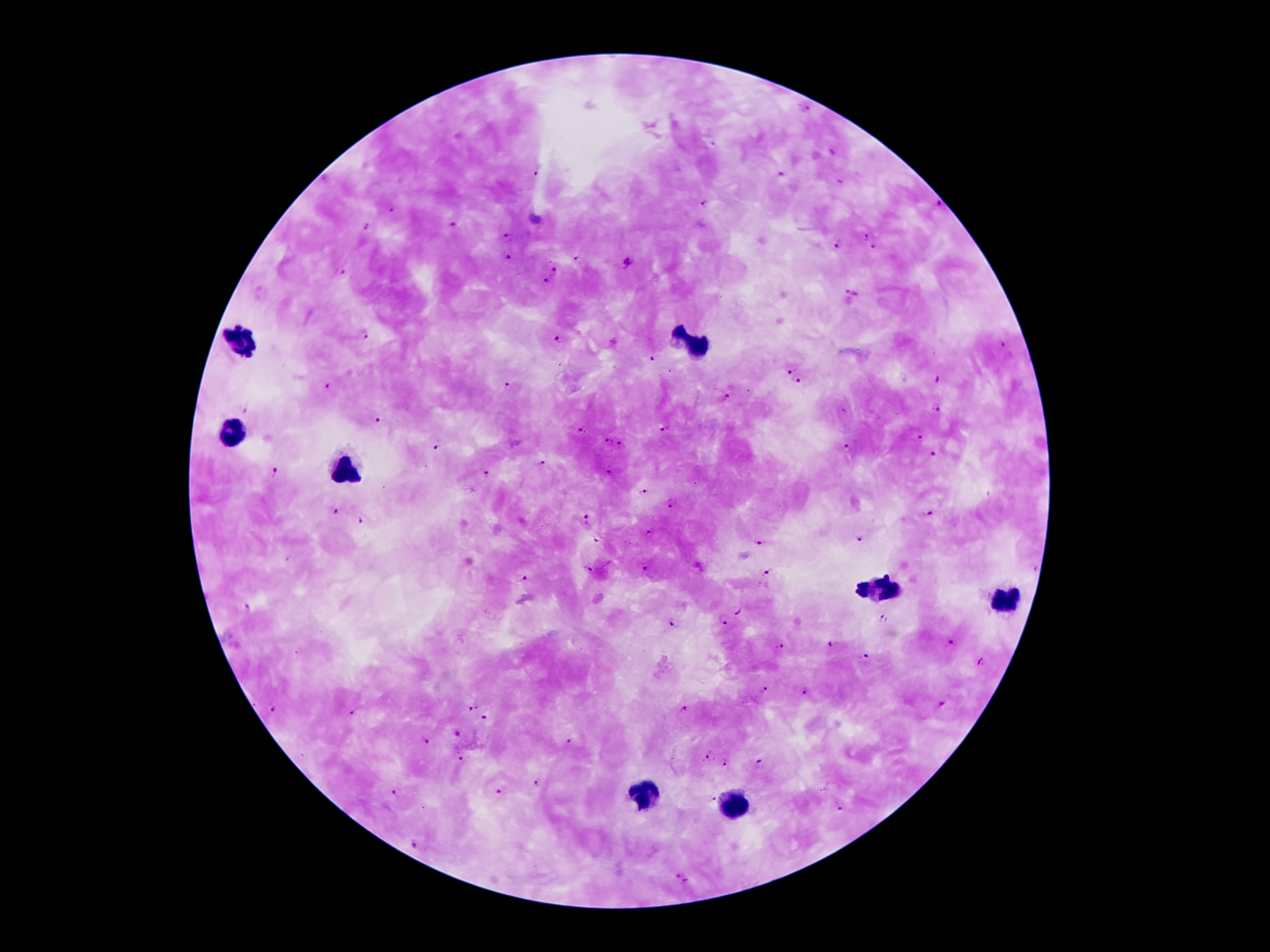
coordinate format = approximate centers as [x, y] in pixels
malaria parasite locations = [804, 109], [539, 170], [780, 173], [705, 204], [939, 205], [392, 210], [455, 226], [367, 228], [509, 236], [866, 239], [837, 246], [874, 248], [508, 257], [577, 259], [627, 265], [554, 270], [340, 274], [546, 281], [851, 294], [366, 337], [561, 341], [1002, 347], [651, 359], [790, 370], [935, 379], [798, 380], [508, 384], [327, 386], [728, 395], [936, 406], [244, 409], [376, 419], [665, 428], [583, 430], [920, 438], [607, 441], [435, 446], [620, 447], [849, 448], [935, 455], [542, 462], [273, 471], [610, 472], [487, 474], [644, 490], [670, 505], [333, 510], [929, 512], [587, 518], [361, 519], [651, 531], [600, 538], [760, 540], [859, 540], [645, 567], [588, 570], [768, 572], [523, 579], [247, 606], [738, 612], [883, 618], [723, 623], [669, 625], [950, 642], [830, 644], [781, 647], [866, 657], [983, 663], [764, 691], [806, 691], [941, 704], [471, 708], [274, 709], [684, 709], [351, 711], [486, 716], [458, 734], [426, 741], [570, 741], [710, 753], [462, 758], [725, 761], [758, 762], [537, 782], [394, 792], [497, 792], [713, 799], [839, 809], [414, 842], [683, 878]
leukocyte locations = [242, 341], [693, 341], [236, 434], [344, 467], [884, 589], [1003, 600], [645, 794], [733, 809]
image size = 1270×952 pixels
magnification = 100x
stain = Giemsa
preparation = thick blood smear
patient malaria status = positive for Plasmodium falciparum
field of view = one from this slide
capture = smartphone camera through the microscope eyepiece